Locate every blood parasite and identify its species.
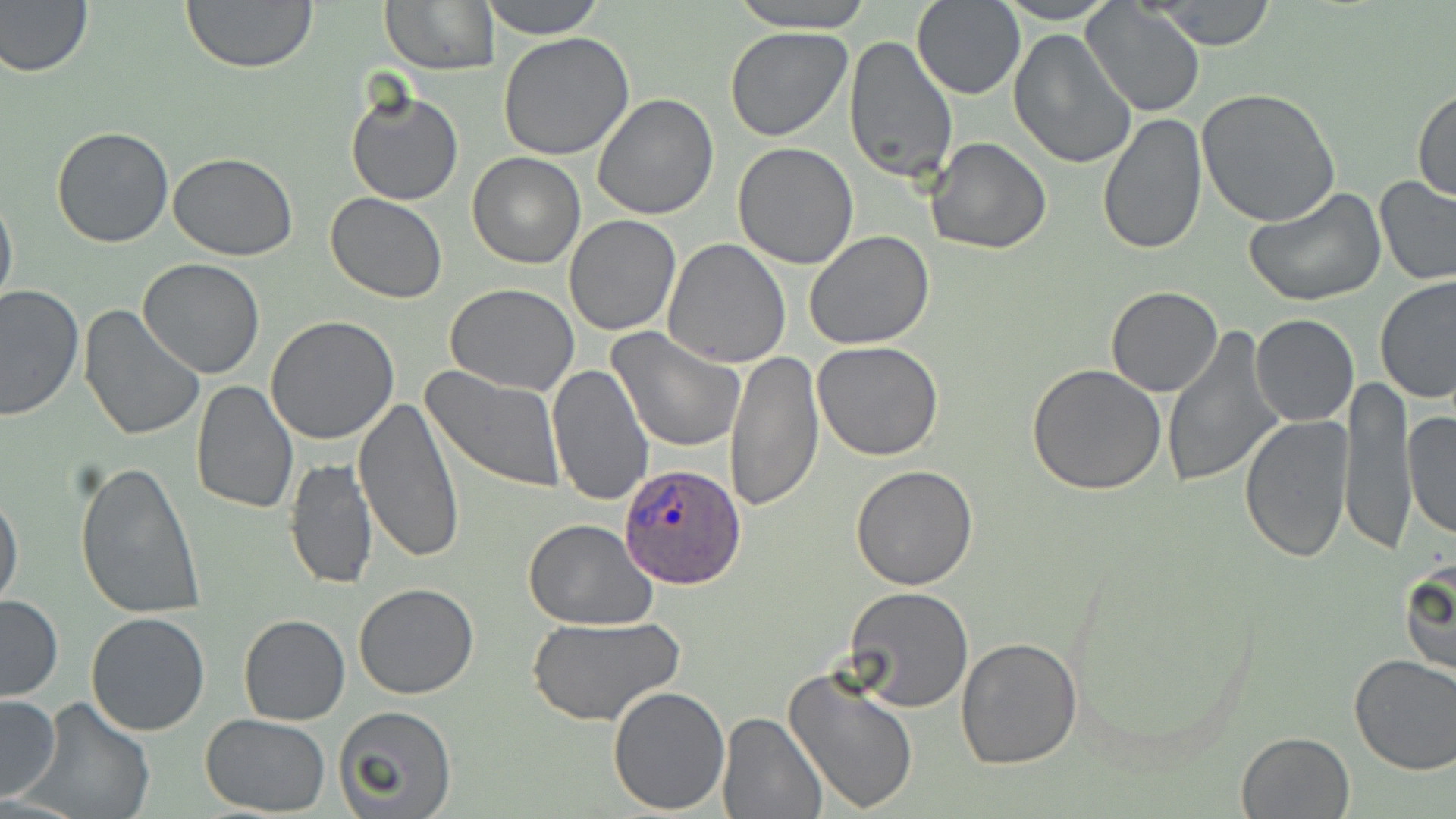

Approximate bounding boxes as (x1,y1)-(x2,y2) corner pairs in pixels.
Plasmodium ovale-infected red blood cells: (617,463)-(745,590).
No Plasmodium falciparum, Plasmodium malariae, Plasmodium vivax, Babesia divergens, or Trypanosoma brucei observed.

Uninfected red blood cell locations: (179,0)-(318,72), (380,0)-(499,74), (478,0)-(608,37), (726,0)-(876,31), (993,0)-(1120,24), (1149,0)-(1281,50), (912,1)-(1027,100), (0,2)-(93,78), (1083,3)-(1206,118), (725,27)-(853,142), (1008,29)-(1137,170), (499,32)-(635,160), (843,34)-(958,184), (1412,86)-(1456,202), (346,89)-(464,206), (1195,89)-(1340,229), (591,93)-(720,220), (1097,111)-(1207,256), (52,126)-(175,247), (925,137)-(1053,255), (733,141)-(859,267), (468,151)-(585,269), (169,152)-(298,259), (1373,177)-(1456,286), (0,187)-(17,314), (1245,187)-(1386,306), (325,194)-(448,305), (564,215)-(682,336), (803,231)-(934,350), (661,239)-(791,369), (138,257)-(266,379), (1376,276)-(1456,407), (445,282)-(581,396), (1,284)-(82,420), (1105,285)-(1223,396), (77,304)-(204,443), (1249,313)-(1359,427), (266,315)-(401,444), (608,328)-(748,453), (1161,329)-(1286,489), (813,341)-(946,461), (724,351)-(824,513), (546,363)-(655,507), (1026,365)-(1168,497), (422,367)-(566,493), (1340,378)-(1417,553), (191,380)-(299,517), (354,395)-(463,565), (1402,410)-(1456,540), (1241,415)-(1355,563), (285,457)-(377,591), (75,462)-(204,618), (850,464)-(980,591), (1,488)-(24,614), (522,518)-(659,631), (1400,553)-(1454,682), (353,583)-(480,700), (845,586)-(976,714), (0,594)-(64,702), (85,611)-(212,737), (239,613)-(350,725), (527,615)-(685,726), (954,635)-(1083,771), (1349,653)-(1456,775), (783,666)-(920,814), (607,684)-(729,814), (0,693)-(62,801), (24,696)-(155,819), (333,707)-(457,818), (717,711)-(827,818), (200,713)-(330,815), (1237,730)-(1354,817). Slide-level diagnosis: Plasmodium ovale. Single field of view. Image is 1456×819 pixels. 1000x magnification. Thin blood film. Optical microscopy. May-Grünwald-Giemsa-stained preparation.